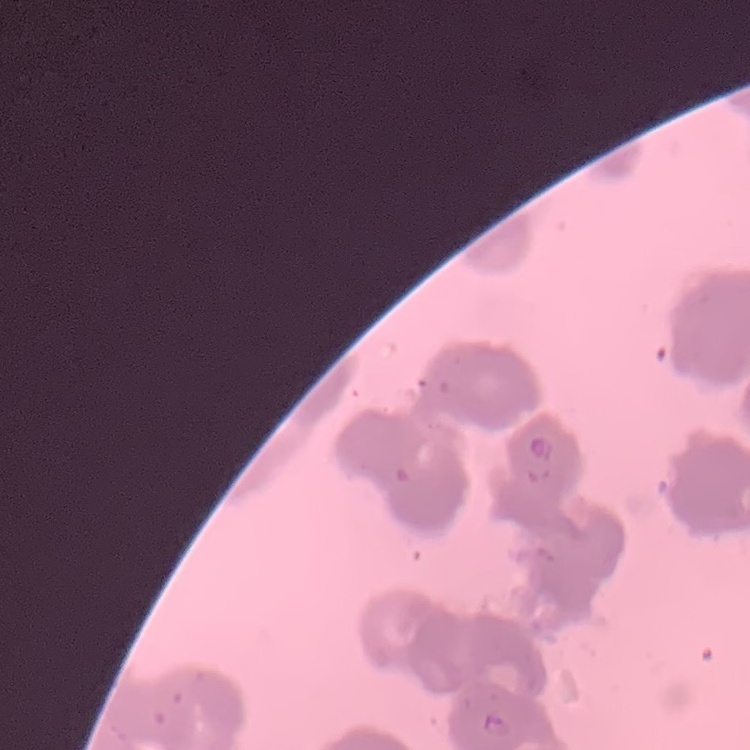
The red blood cells exhibit rouleaux formation. One tile cut from a larger photomicrograph. Thin blood film. Field's or Giemsa stain.